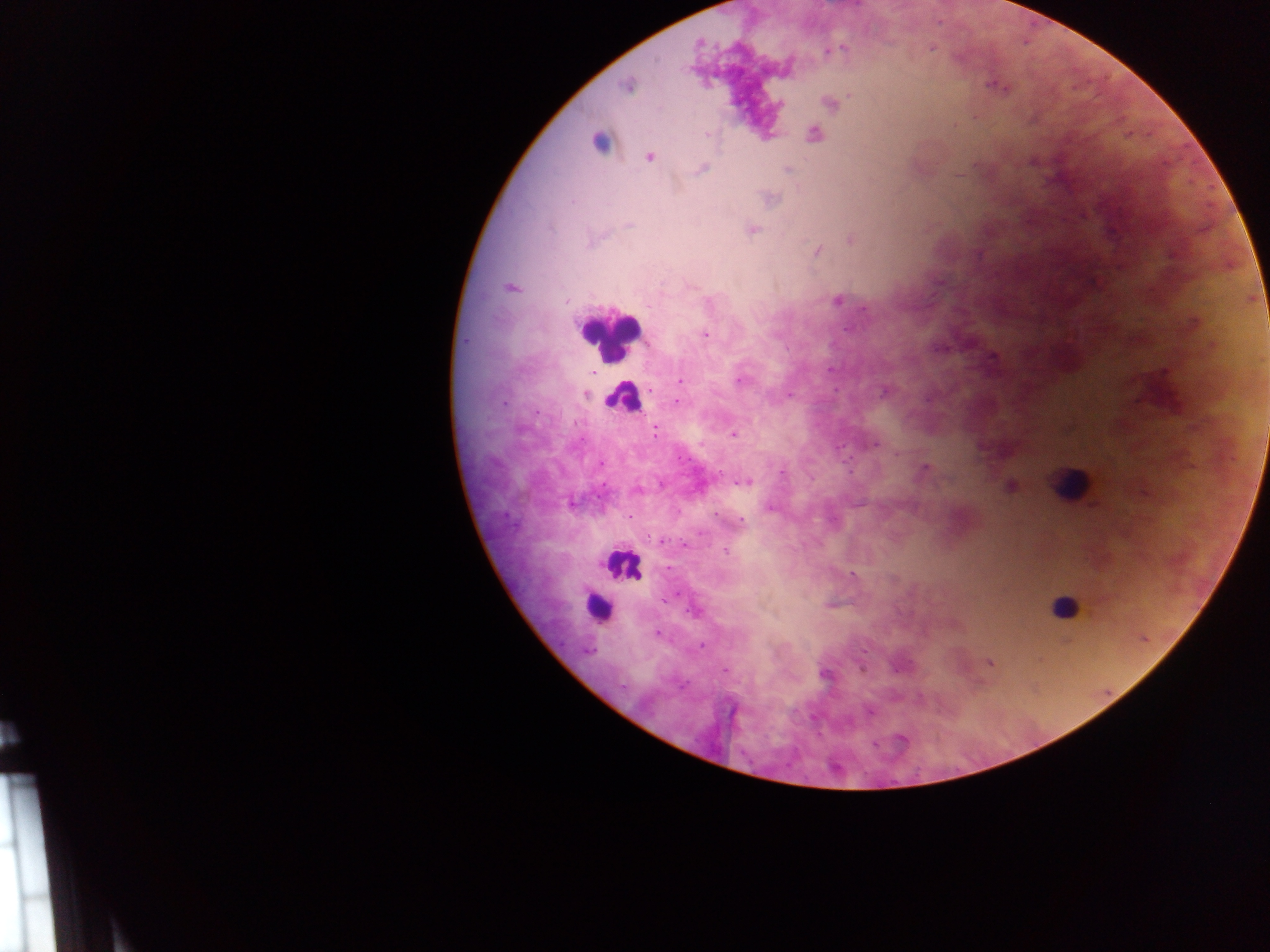
leukocyte locations = approximate centers as (x, y) in pixels: (599, 143), (609, 334), (623, 398), (1069, 484), (621, 566), (597, 606), (1064, 606)
country = Ghana
field of view = single
capture = mobile-phone photograph through a microscope
preparation = thick blood film
image size = 1270×952 pixels
malaria parasite locations = approximate centers as (x, y) in pixels: (698, 44), (842, 49), (627, 86), (1000, 87), (830, 103), (780, 104), (813, 134), (707, 135), (649, 158), (701, 169), (788, 169), (629, 225), (752, 230), (851, 240), (818, 252), (511, 287), (565, 300), (837, 301), (648, 305), (865, 309), (704, 334), (994, 357), (591, 373), (739, 380), (680, 381), (651, 389), (884, 392), (586, 395), (789, 395), (677, 402), (656, 432), (732, 435), (874, 444), (925, 468), (782, 473), (745, 483), (1010, 486), (572, 504), (770, 508), (629, 516), (741, 522), (661, 541), (726, 551), (853, 576), (692, 612), (657, 634), (701, 646), (863, 652), (989, 662), (862, 668), (726, 669), (824, 675), (870, 712), (902, 739), (875, 743)